Assess this cell for malaria.
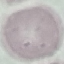

Uninfected.

Photographed with a smartphone camera at the microscope eyepiece. Thin smear of blood. Giemsa stain. Cell patch, automatically extracted from a larger field of view and resized to 64 × 64 pixels.